Give the position of every Plasmodium parasite visible.
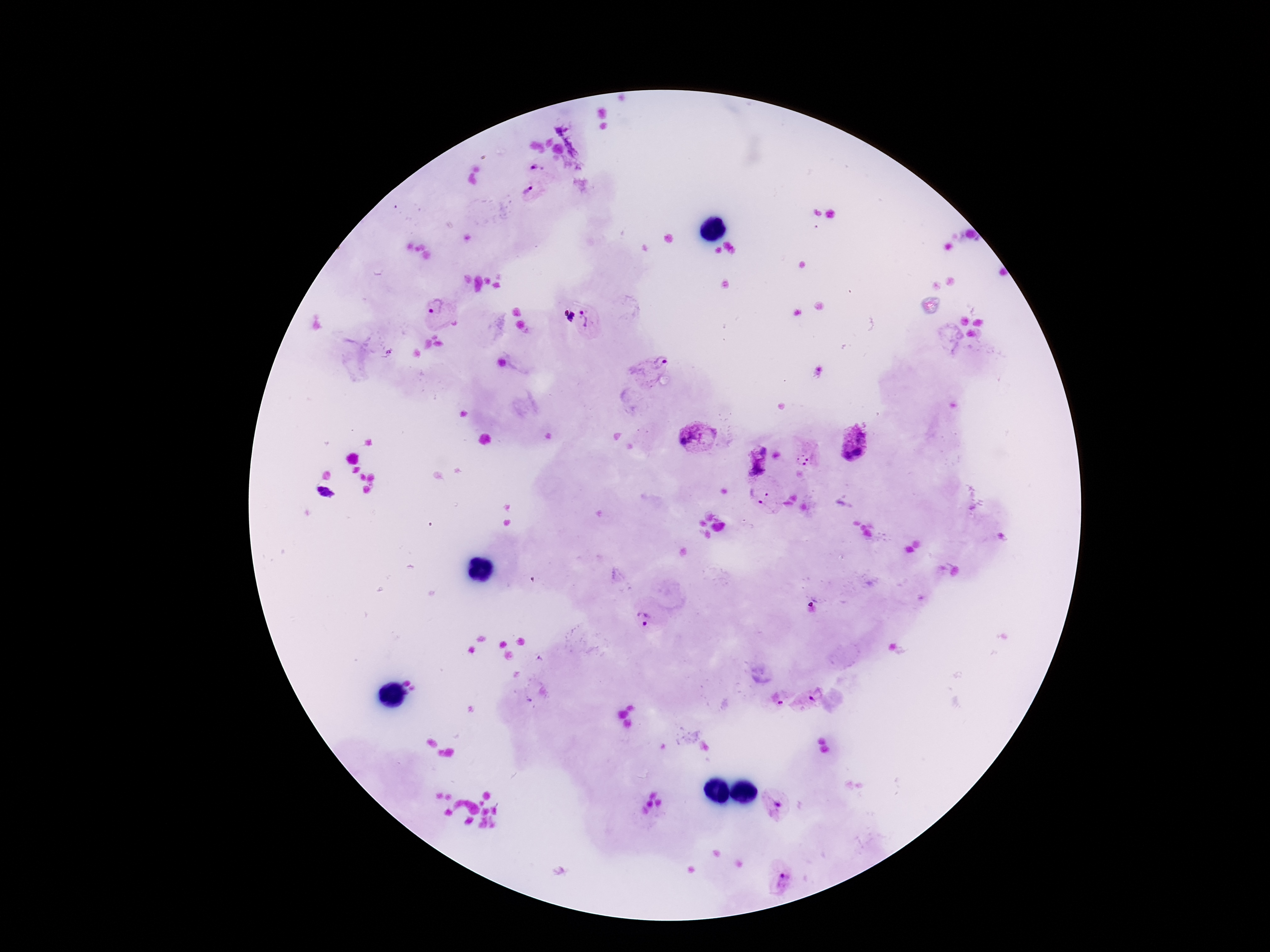
Approximate centers as [x, y] in pixels.
Plasmodium parasites: [566, 142], [535, 167], [528, 191], [436, 307], [569, 317], [590, 318], [649, 364], [696, 437], [855, 444], [758, 460], [804, 460], [759, 490], [322, 492], [766, 510], [644, 617], [817, 696], [785, 698], [774, 807], [781, 882].

Image is 1270×952 pixels. 100x magnification. Thick peripheral-blood smear. Smartphone photograph taken through the microscope eyepiece. Single field of view. Giemsa stain. Patient malaria status: infected.